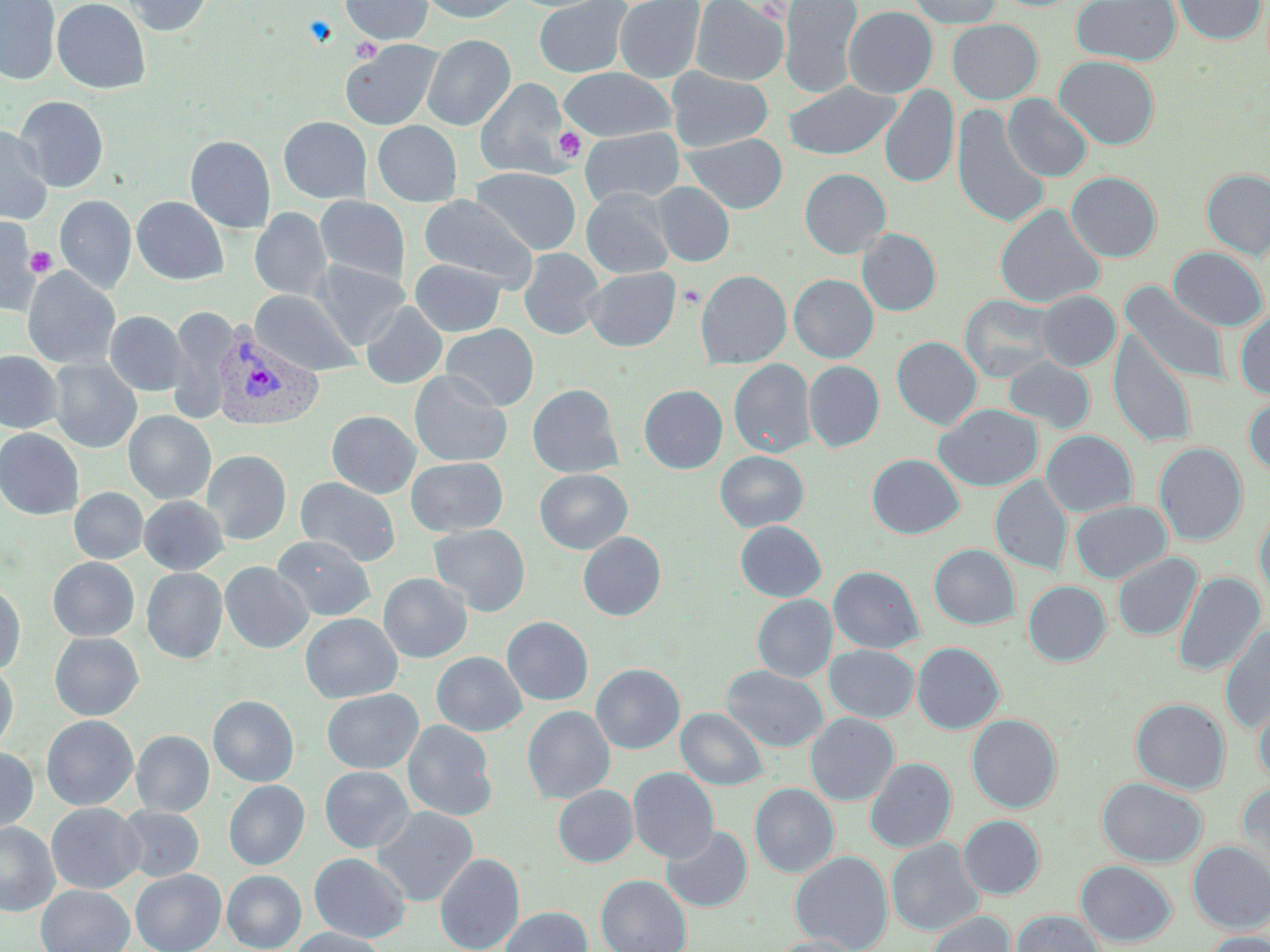 Approximate bounding boxes as (x1, y1, x2, y2) in pixels. Plasmodium vivax-infected red blood cell locations: (211, 321, 324, 432). Platelet locations: (553, 126, 586, 163), (26, 244, 57, 281), (677, 285, 705, 310). Uninfected red blood cell locations: (1, 0, 61, 85), (52, 0, 151, 93), (121, 0, 214, 36), (340, 0, 434, 45), (417, 0, 523, 23), (533, 0, 633, 78), (614, 0, 705, 83), (690, 0, 788, 85), (779, 0, 863, 99), (906, 0, 1003, 28), (1071, 0, 1181, 66), (1173, 0, 1266, 45), (843, 6, 938, 98), (947, 19, 1043, 104), (422, 34, 515, 131), (340, 40, 442, 131), (1055, 56, 1160, 150), (558, 67, 676, 142), (666, 67, 773, 152), (475, 78, 572, 179), (782, 80, 901, 160), (879, 84, 959, 189), (1003, 94, 1093, 182), (14, 96, 109, 193), (951, 104, 1050, 230), (278, 116, 371, 204), (372, 120, 462, 207), (0, 126, 53, 224), (580, 127, 685, 207), (682, 133, 788, 213), (185, 135, 275, 233), (471, 167, 581, 255), (799, 168, 891, 258), (1201, 168, 1270, 261), (1066, 171, 1162, 262), (652, 182, 735, 267), (581, 189, 674, 278), (418, 194, 539, 290), (55, 195, 136, 295), (131, 196, 228, 285), (315, 196, 410, 285), (995, 203, 1104, 308), (250, 207, 332, 301), (0, 217, 42, 316), (857, 228, 941, 315), (1168, 247, 1268, 331), (518, 248, 605, 340), (410, 258, 505, 336), (311, 260, 409, 349), (584, 266, 681, 351), (22, 267, 121, 370), (695, 270, 792, 369), (789, 274, 878, 363), (1122, 283, 1229, 385), (250, 290, 362, 377), (1036, 290, 1121, 371), (960, 294, 1058, 383), (361, 301, 447, 389), (167, 307, 236, 422), (105, 310, 187, 396), (1234, 311, 1270, 400), (441, 324, 539, 411), (1108, 329, 1197, 449), (891, 336, 982, 430), (0, 351, 62, 433), (1003, 355, 1095, 434), (48, 358, 142, 453), (728, 359, 816, 457), (803, 360, 884, 452), (409, 370, 512, 467), (527, 383, 623, 478), (638, 384, 728, 473), (1243, 395, 1270, 477), (934, 403, 1043, 491), (326, 410, 421, 498), (123, 411, 216, 504), (0, 428, 84, 520), (1041, 430, 1138, 517), (1154, 442, 1248, 546), (202, 450, 291, 544), (715, 450, 809, 532), (867, 454, 965, 538), (406, 456, 508, 537), (534, 469, 632, 554), (990, 476, 1073, 575), (295, 477, 401, 567), (69, 487, 147, 564), (139, 495, 229, 575), (1070, 500, 1172, 583), (1255, 504, 1270, 599), (735, 520, 826, 601), (429, 523, 531, 616), (578, 531, 666, 621), (272, 535, 376, 621), (929, 544, 1019, 630), (1112, 551, 1202, 641), (47, 557, 139, 641), (219, 561, 313, 653), (828, 566, 924, 654), (141, 567, 227, 664), (1173, 571, 1266, 676), (378, 573, 472, 663), (1023, 580, 1111, 666), (0, 583, 26, 676), (752, 594, 837, 682), (300, 612, 403, 703), (502, 616, 593, 705), (1220, 625, 1270, 734), (49, 632, 144, 720), (911, 642, 1004, 734), (824, 645, 920, 723), (431, 651, 527, 736), (0, 662, 19, 755), (591, 663, 685, 754), (721, 665, 828, 752), (322, 689, 423, 774), (208, 695, 299, 787), (1131, 698, 1230, 794), (1253, 699, 1270, 786), (522, 705, 615, 805), (677, 707, 769, 791), (805, 712, 899, 805), (967, 714, 1062, 813), (41, 715, 138, 811), (402, 720, 497, 822), (131, 730, 214, 817), (0, 746, 38, 836), (865, 757, 956, 853), (319, 766, 415, 853), (628, 767, 719, 863), (1097, 777, 1207, 867), (223, 780, 309, 870), (1238, 781, 1270, 879), (750, 783, 838, 878), (553, 785, 638, 867), (46, 803, 144, 894), (117, 806, 204, 882), (372, 806, 478, 907), (958, 815, 1045, 899), (0, 822, 59, 916), (662, 824, 751, 912), (886, 837, 984, 936), (1188, 841, 1270, 934), (790, 850, 893, 952), (435, 852, 524, 952), (309, 853, 411, 943), (1075, 860, 1176, 947), (130, 869, 226, 952), (222, 870, 306, 952), (596, 874, 692, 952), (35, 885, 135, 952), (500, 906, 592, 952), (1011, 910, 1106, 952), (926, 911, 1016, 952), (288, 927, 387, 952), (1200, 930, 1270, 952), (771, 936, 861, 952). Slide-level diagnosis: Plasmodium vivax. 1000x magnification. May-Grünwald-Giemsa stain. Optical microscopy. One field of a larger specimen. Image is 1270×952 pixels. Thin blood film.